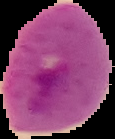
preparation = thin blood film
image size = 115×139 pixels
image type = cell region segmented out of the field of view; surrounding area masked to black
result = Plasmodium parasites identified